Assess this cell for malaria.
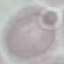
Uninfected.

preparation = thin smear
image type = cell patch, automatically extracted from a larger field of view and resized to 64 × 64 pixels
capture = smartphone camera at the microscope eyepiece
stain = Giemsa